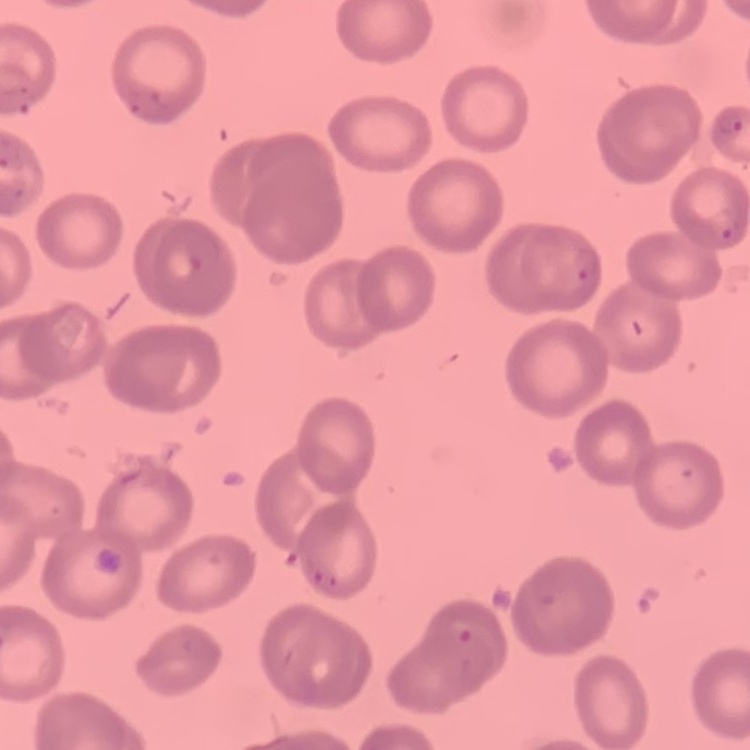

erythrocyte morphology = no rouleaux formation
image type = square crop of a larger photomicrograph
stain = Field's or Giemsa
preparation = thin blood film